Point out each malaria parasite.
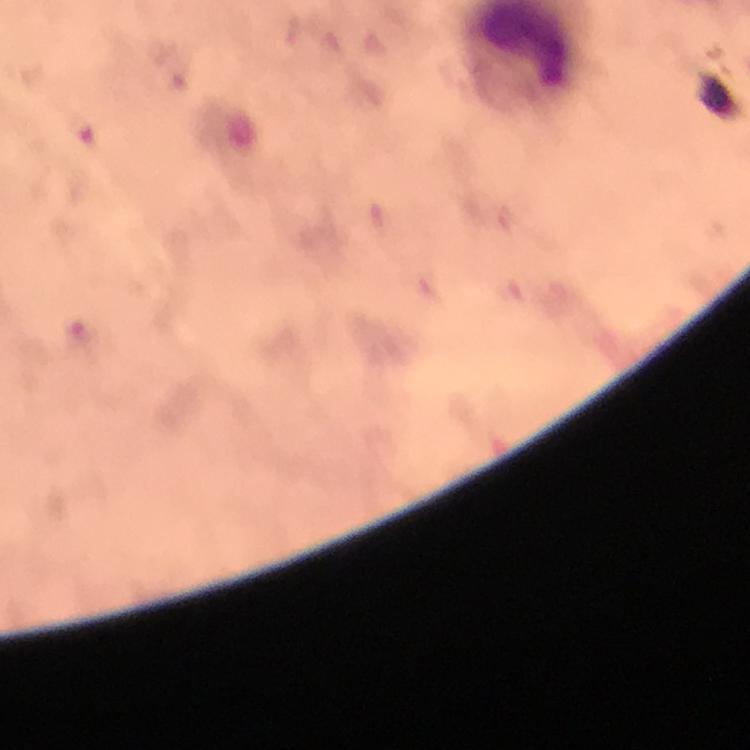

Approximate centers as [x, y] in pixels.
Malaria parasites: [81, 129].

Giemsa stain. Immersion oil was used. Smartphone photograph taken through a microscope. From a diagnostic examination for malaria. Thick smear. 100x magnification. Image is 750×750 pixels. A crop from one field of view.